Locate and identify every blood parasite.
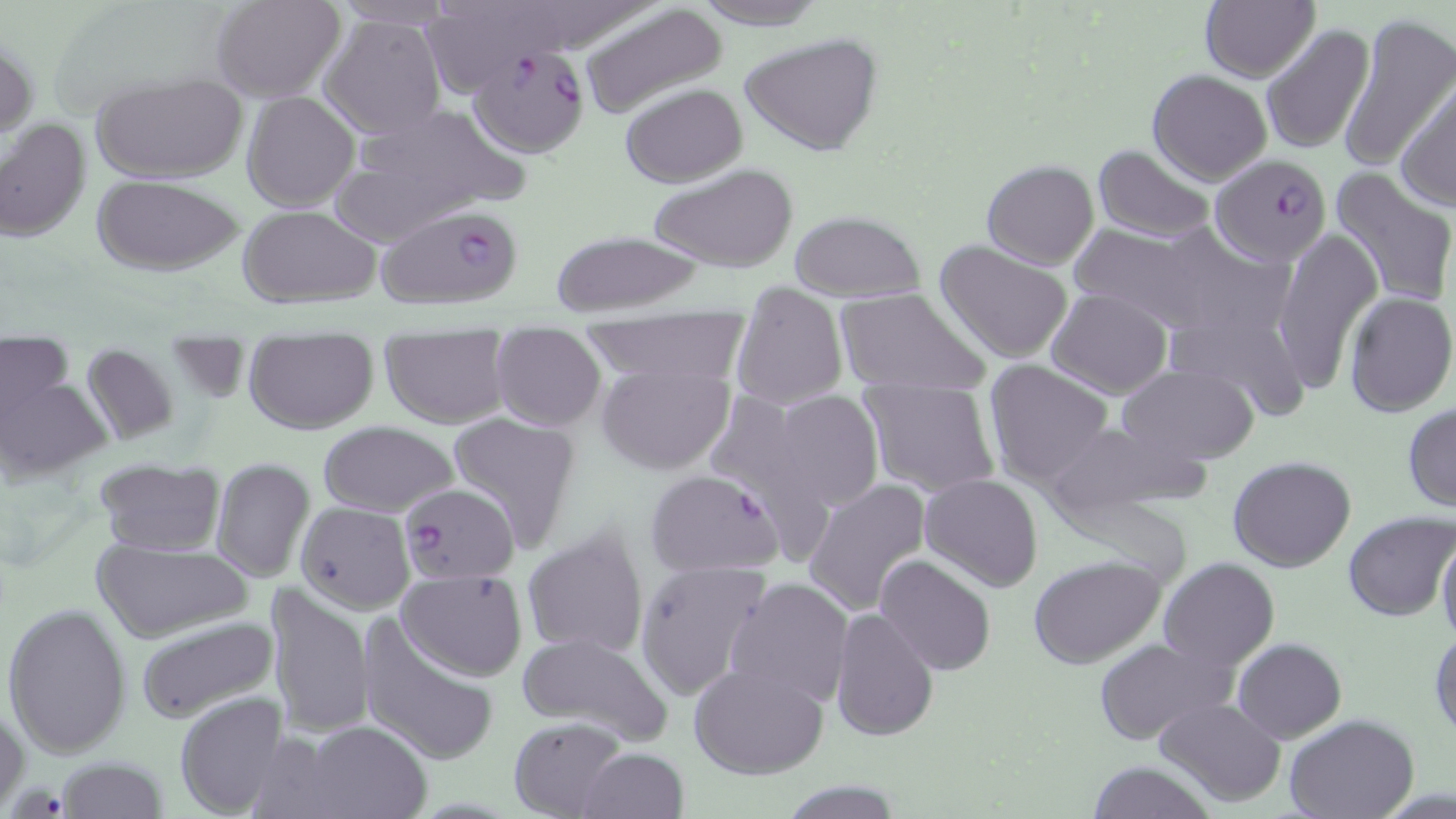
Approximate bounding boxes as (x1, y1, x2, y2) in pixels.
Plasmodium falciparum-infected red blood cells: (469, 44, 589, 157), (1210, 153, 1333, 266), (377, 201, 525, 311), (645, 469, 783, 578), (409, 485, 527, 586).
No Plasmodium ovale, Plasmodium malariae, Plasmodium vivax, Babesia divergens, or Trypanosoma brucei observed.

Summary:
  - Uninfected red blood cell locations: (211, 0, 346, 102), (328, 0, 458, 29), (687, 0, 831, 28), (423, 2, 562, 98), (1199, 2, 1319, 82), (580, 3, 727, 118), (1336, 12, 1454, 174), (320, 14, 446, 140), (1261, 23, 1377, 156), (739, 32, 884, 156), (1, 39, 37, 140), (1147, 69, 1273, 185), (93, 73, 248, 184), (1396, 78, 1455, 210), (621, 83, 748, 186), (242, 91, 360, 211), (340, 102, 525, 230), (1, 117, 91, 245), (1093, 144, 1215, 241), (981, 160, 1100, 269), (648, 163, 797, 272), (1328, 167, 1456, 308), (91, 175, 247, 275), (237, 206, 381, 307), (790, 211, 928, 302), (1071, 221, 1260, 337), (1273, 227, 1382, 389), (547, 230, 711, 316), (935, 238, 1073, 363), (731, 286, 847, 410), (834, 287, 990, 397), (1045, 288, 1171, 398), (1343, 292, 1456, 418), (1164, 300, 1313, 422), (581, 313, 752, 385), (2, 328, 79, 447), (489, 330, 606, 432), (380, 333, 510, 429), (243, 336, 380, 435), (81, 343, 180, 445), (0, 359, 102, 483), (984, 361, 1113, 486), (596, 362, 735, 475), (1119, 363, 1257, 465), (858, 378, 1001, 499), (769, 392, 884, 513), (1403, 402, 1456, 512), (446, 412, 584, 552), (1037, 420, 1200, 526), (316, 421, 460, 517), (1228, 456, 1357, 573), (209, 457, 316, 583), (95, 459, 223, 556), (920, 474, 1043, 593), (803, 479, 930, 617), (295, 500, 414, 612), (1342, 511, 1455, 622), (522, 527, 650, 659), (1435, 532, 1456, 649), (90, 536, 255, 643), (875, 554, 996, 676), (1026, 555, 1169, 672), (1158, 557, 1278, 671), (633, 560, 771, 701), (398, 570, 528, 679), (725, 577, 853, 708), (264, 584, 372, 740), (3, 601, 132, 758), (829, 606, 939, 742), (357, 615, 501, 768), (135, 616, 277, 724), (1429, 627, 1456, 741), (517, 633, 670, 750), (1094, 636, 1232, 746), (1232, 637, 1346, 742), (689, 662, 829, 780), (173, 692, 293, 816), (1153, 697, 1285, 806), (0, 703, 29, 814), (1284, 714, 1421, 819), (509, 716, 628, 819), (291, 720, 433, 818), (577, 747, 688, 819), (58, 756, 168, 819), (1085, 761, 1216, 819), (781, 780, 904, 818)
  - Slide-level diagnosis: Plasmodium falciparum
  - Modality: light microscopy
  - Image size: 1456×819 pixels
  - Magnification: 1000x
  - Preparation: thin blood smear
  - Field of view: one of a larger specimen
  - Stain: May-Grünwald-Giemsa